Classify this cell by malaria status.
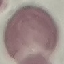
Uninfected.

preparation: thin blood smear
stain: Giemsa
capture: smartphone camera at the microscope eyepiece
image_type: cell patch, automatically extracted from a larger field of view and resized to 64 × 64 pixels